Assess this cell for malaria.
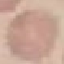

Uninfected.

Acquired by smartphone through the microscope eyepiece. Cell patch, automatically extracted from a larger field of view and resized to 64 × 64 pixels. Giemsa stain. Thin blood film.